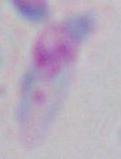
modality: micrograph
identification: Toxoplasma gondii
magnification: 1000x